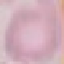

Summary:
  - Result: no malaria parasites detected
  - Image type: automatically extracted cell patch, resized to 64 × 64 pixels
  - Stain: Giemsa
  - Capture: smartphone camera at the microscope eyepiece
  - Preparation: thin blood smear